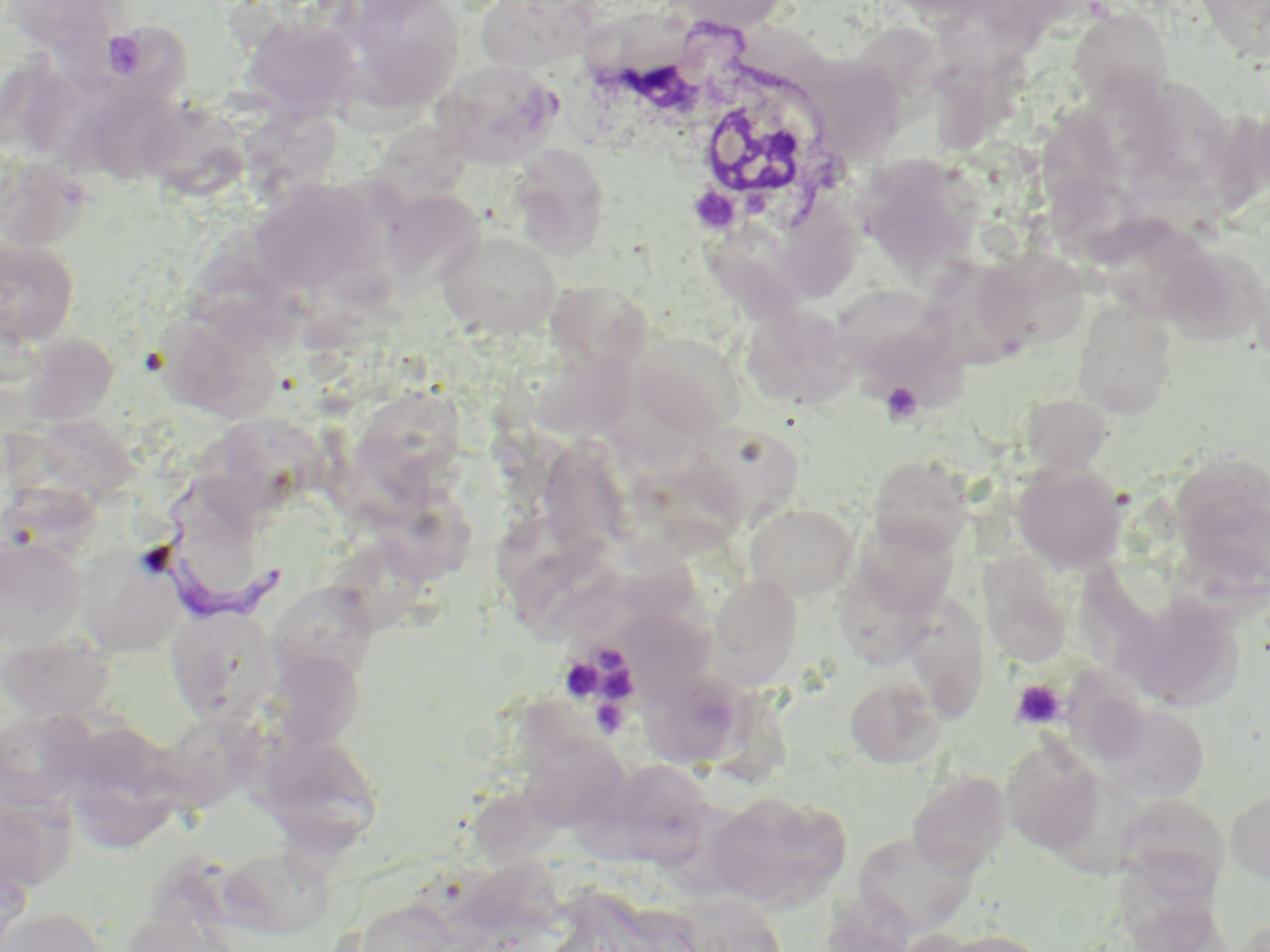 Approximate bounding boxes as named x1/y1/x2/y2 corners in pixels. White blood cell locations: (x1=578, y1=26, x2=841, y2=232). Trypanosoma brucei locations: (x1=142, y1=482, x2=288, y2=623). Platelet locations: (x1=102, y1=29, x2=149, y2=80), (x1=881, y1=382, x2=922, y2=424), (x1=597, y1=642, x2=632, y2=676), (x1=561, y1=654, x2=603, y2=703), (x1=604, y1=668, x2=636, y2=709), (x1=1010, y1=679, x2=1067, y2=729), (x1=592, y1=701, x2=629, y2=737). Uninfected red blood cell locations: (x1=1, y1=0, x2=132, y2=56), (x1=336, y1=0, x2=464, y2=111), (x1=476, y1=0, x2=600, y2=72), (x1=664, y1=0, x2=792, y2=32), (x1=1192, y1=0, x2=1270, y2=62), (x1=1068, y1=7, x2=1175, y2=110), (x1=240, y1=17, x2=362, y2=120), (x1=71, y1=23, x2=200, y2=112), (x1=431, y1=59, x2=563, y2=167), (x1=28, y1=67, x2=123, y2=180), (x1=1133, y1=84, x2=1242, y2=197), (x1=90, y1=94, x2=185, y2=192), (x1=146, y1=107, x2=257, y2=198), (x1=1036, y1=107, x2=1131, y2=220), (x1=509, y1=144, x2=612, y2=258), (x1=854, y1=154, x2=982, y2=276), (x1=1, y1=155, x2=92, y2=251), (x1=250, y1=175, x2=383, y2=299), (x1=782, y1=192, x2=867, y2=298), (x1=383, y1=196, x2=494, y2=304), (x1=1096, y1=215, x2=1219, y2=316), (x1=436, y1=229, x2=563, y2=339), (x1=0, y1=236, x2=80, y2=348), (x1=180, y1=249, x2=315, y2=350), (x1=979, y1=250, x2=1094, y2=355), (x1=1159, y1=252, x2=1263, y2=347), (x1=930, y1=261, x2=1036, y2=376), (x1=535, y1=281, x2=653, y2=369), (x1=833, y1=284, x2=947, y2=378), (x1=1072, y1=298, x2=1177, y2=420), (x1=741, y1=305, x2=858, y2=410), (x1=149, y1=319, x2=286, y2=425), (x1=633, y1=332, x2=746, y2=437), (x1=21, y1=333, x2=118, y2=426), (x1=538, y1=344, x2=650, y2=444), (x1=345, y1=388, x2=469, y2=510), (x1=1021, y1=395, x2=1112, y2=475), (x1=39, y1=422, x2=153, y2=508), (x1=686, y1=422, x2=805, y2=533), (x1=192, y1=424, x2=329, y2=519), (x1=538, y1=437, x2=629, y2=570), (x1=630, y1=453, x2=750, y2=560), (x1=868, y1=455, x2=972, y2=555), (x1=1170, y1=455, x2=1270, y2=588), (x1=1013, y1=462, x2=1126, y2=572), (x1=374, y1=491, x2=475, y2=585), (x1=744, y1=502, x2=859, y2=600), (x1=500, y1=514, x2=617, y2=617), (x1=851, y1=517, x2=960, y2=618), (x1=1, y1=533, x2=88, y2=652), (x1=77, y1=542, x2=183, y2=657), (x1=323, y1=545, x2=434, y2=639), (x1=980, y1=556, x2=1073, y2=666), (x1=838, y1=563, x2=939, y2=666), (x1=708, y1=574, x2=803, y2=684), (x1=274, y1=577, x2=372, y2=686), (x1=913, y1=588, x2=993, y2=722), (x1=1122, y1=595, x2=1245, y2=711), (x1=165, y1=604, x2=281, y2=725), (x1=618, y1=619, x2=718, y2=712), (x1=0, y1=632, x2=117, y2=721), (x1=266, y1=654, x2=371, y2=752), (x1=632, y1=660, x2=756, y2=775), (x1=1062, y1=663, x2=1159, y2=771), (x1=844, y1=675, x2=945, y2=768), (x1=1092, y1=698, x2=1210, y2=803), (x1=1, y1=707, x2=96, y2=814), (x1=56, y1=721, x2=184, y2=851), (x1=157, y1=722, x2=274, y2=820), (x1=253, y1=725, x2=384, y2=856), (x1=517, y1=731, x2=629, y2=829), (x1=1001, y1=736, x2=1106, y2=856), (x1=623, y1=760, x2=715, y2=877), (x1=906, y1=770, x2=1012, y2=875), (x1=1225, y1=788, x2=1270, y2=884), (x1=477, y1=791, x2=566, y2=863), (x1=706, y1=791, x2=850, y2=911), (x1=1114, y1=793, x2=1230, y2=896), (x1=853, y1=830, x2=980, y2=936), (x1=222, y1=847, x2=337, y2=938), (x1=347, y1=898, x2=462, y2=952), (x1=2, y1=907, x2=109, y2=952), (x1=118, y1=908, x2=239, y2=952), (x1=930, y1=927, x2=1053, y2=952). Slide-level diagnosis: Trypanosoma brucei. Optical microscopy. One field of a larger specimen. Image is 1270×952 pixels. Thin blood film. May-Grünwald-Giemsa-stained preparation. Captured at 1000x magnification.